Report the malaria status of this cell.
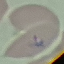

Parasitized.

Photographed with a smartphone camera at the microscope eyepiece. Thin blood smear. Giemsa-stained preparation. Cell patch, automatically extracted from a larger field of view and resized to 64 × 64 pixels.